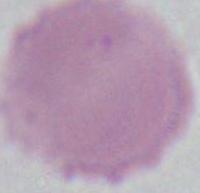

modality = micrograph
identification = erythrocyte
magnification = 1000x